Assess the morphology of the erythrocytes.
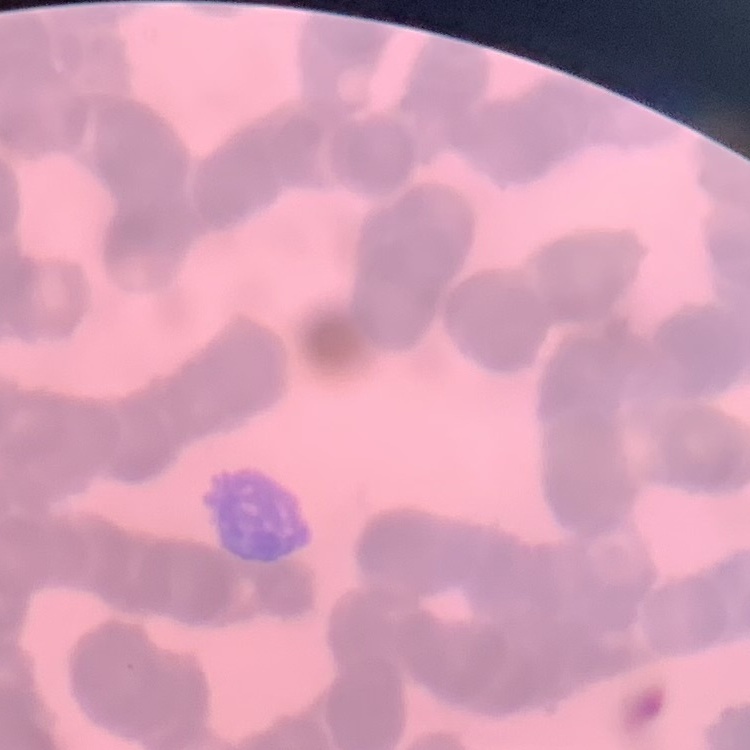
Rouleaux formation.

Summary:
  - Stain: Field's or Giemsa
  - Image type: square crop of a larger photomicrograph
  - Preparation: thin peripheral smear